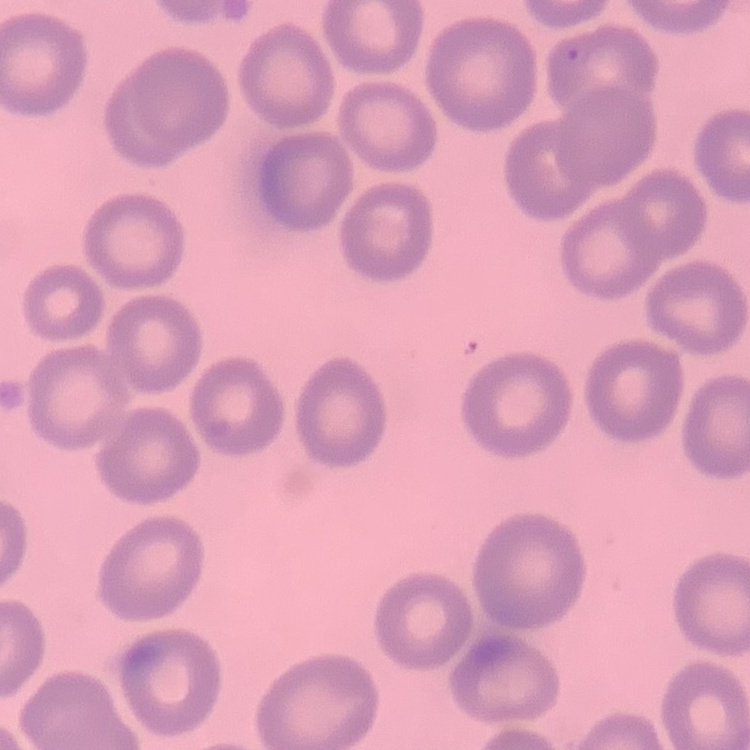
The red blood cells show no rouleaux formation. Stained with either Field's or Giemsa. One tile cut from a larger photomicrograph. Thin blood film.